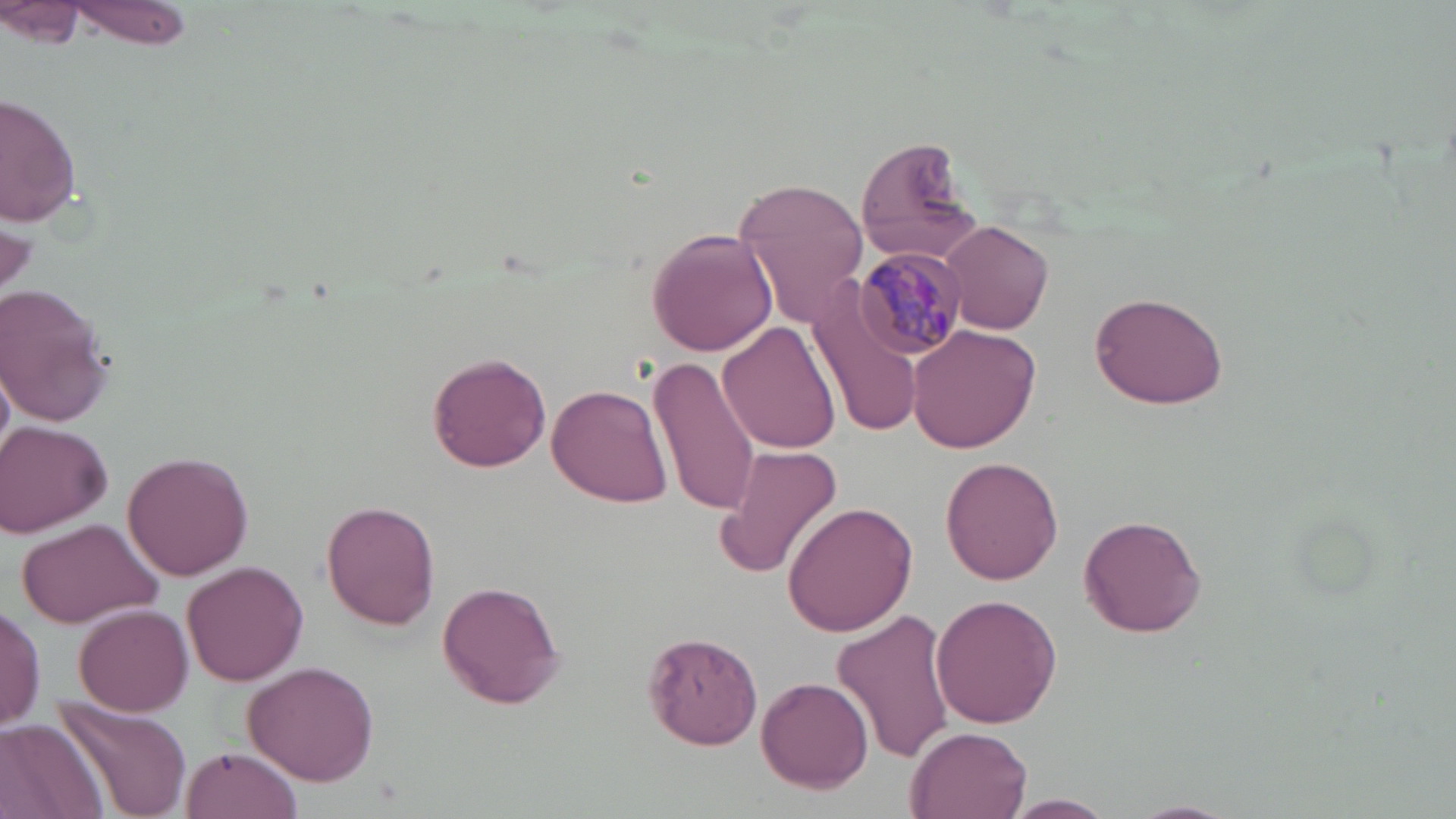

Approximate bounding boxes as (x1,y1)-(x2,y2) corner pairs in pixels. Plasmodium malariae-infected red blood cell locations: (857,248)-(970,361). Uninfected red blood cell locations: (64,0)-(194,47), (5,3)-(85,46), (0,95)-(81,229), (853,134)-(985,266), (733,176)-(870,330), (1,208)-(34,309), (939,220)-(1054,334), (647,228)-(779,356), (808,280)-(924,438), (0,283)-(115,425), (1089,289)-(1230,410), (907,321)-(1042,452), (719,322)-(841,454), (426,351)-(552,472), (649,352)-(763,518), (2,365)-(16,453), (545,382)-(675,507), (1,421)-(115,536), (716,446)-(844,580), (121,451)-(255,580), (941,456)-(1064,585), (321,500)-(438,629), (782,500)-(918,636), (15,515)-(165,629), (1078,515)-(1207,638), (183,559)-(308,685), (435,579)-(566,709), (929,594)-(1062,728), (0,602)-(46,734), (73,603)-(193,714), (833,605)-(954,766), (640,633)-(764,750), (243,660)-(380,787), (755,678)-(874,792), (54,699)-(192,817), (0,718)-(107,819), (903,725)-(1033,819), (179,746)-(302,818), (1004,794)-(1116,817), (1128,799)-(1241,818). Slide-level diagnosis: Plasmodium malariae. Captured at 1000x magnification. Image is 1456×819 pixels. Single field of view. Optical microscopy. Thin blood film. May-Grünwald-Giemsa-stained preparation.